Describe the morphology of the erythrocytes.
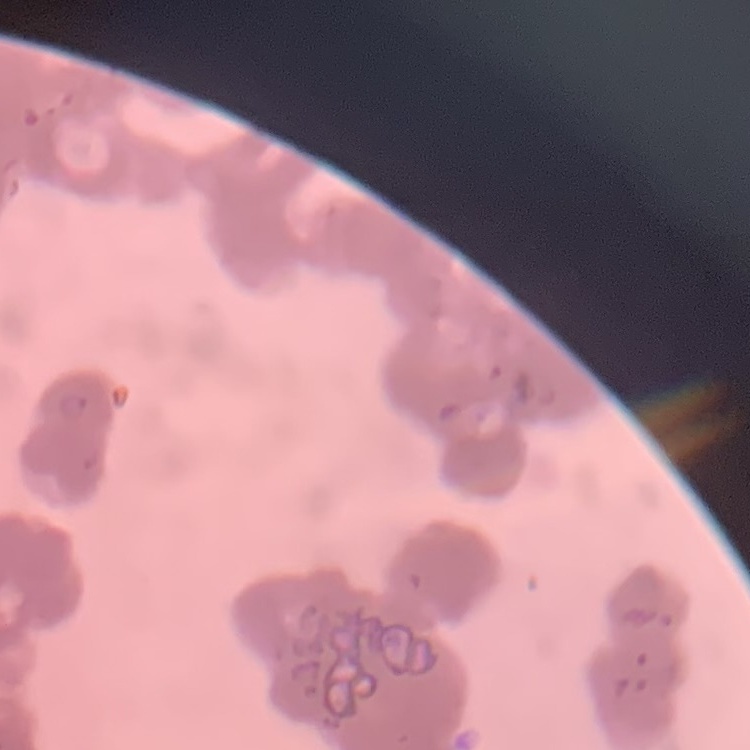

They show rouleaux formation.

Summary:
  - Image type: one tile cut from a larger photomicrograph
  - Stain: Field's or Giemsa
  - Preparation: thin blood smear